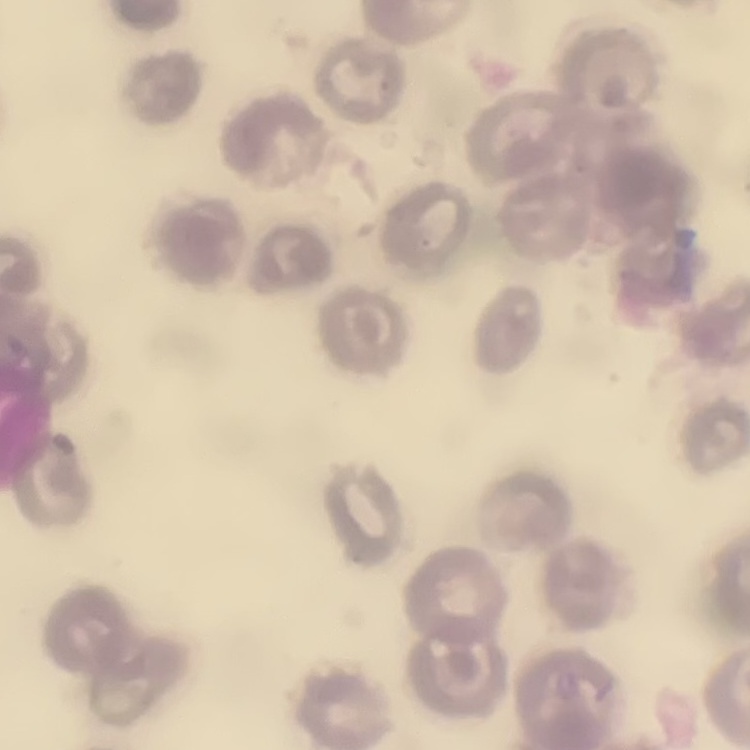

The red blood cells show no rouleaux formation. Thin blood film. Square crop of a larger photomicrograph. Field's or Giemsa stain.